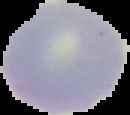

image_type: segmented cell region on a black background
image_size: 130×115 pixels
preparation: thin blood smear
malaria_status: uninfected